Report the malaria status of this cell.
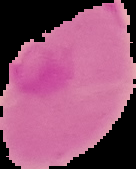
It is uninfected.

Image is 136×169 pixels. From a thin blood smear. Segmented cell region on a black background.